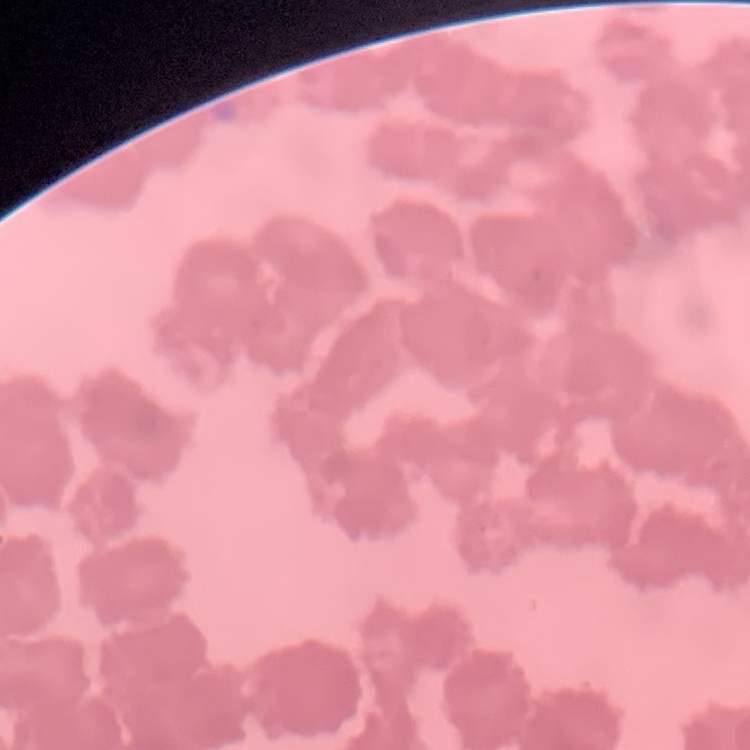
red blood cell morphology = rouleaux formation
preparation = thin blood film
stain = Field's or Giemsa
image type = square crop of a larger photomicrograph